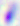

400x magnification. Toxoplasma gondii is shown. Micrograph.